Report the malaria status of this cell.
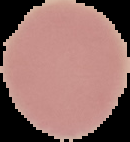
Uninfected.

From a thin blood smear. Image is 130×142 pixels. Cell region segmented out of the field of view; the surrounding area is masked to black.